Locate every Plasmodium parasite.
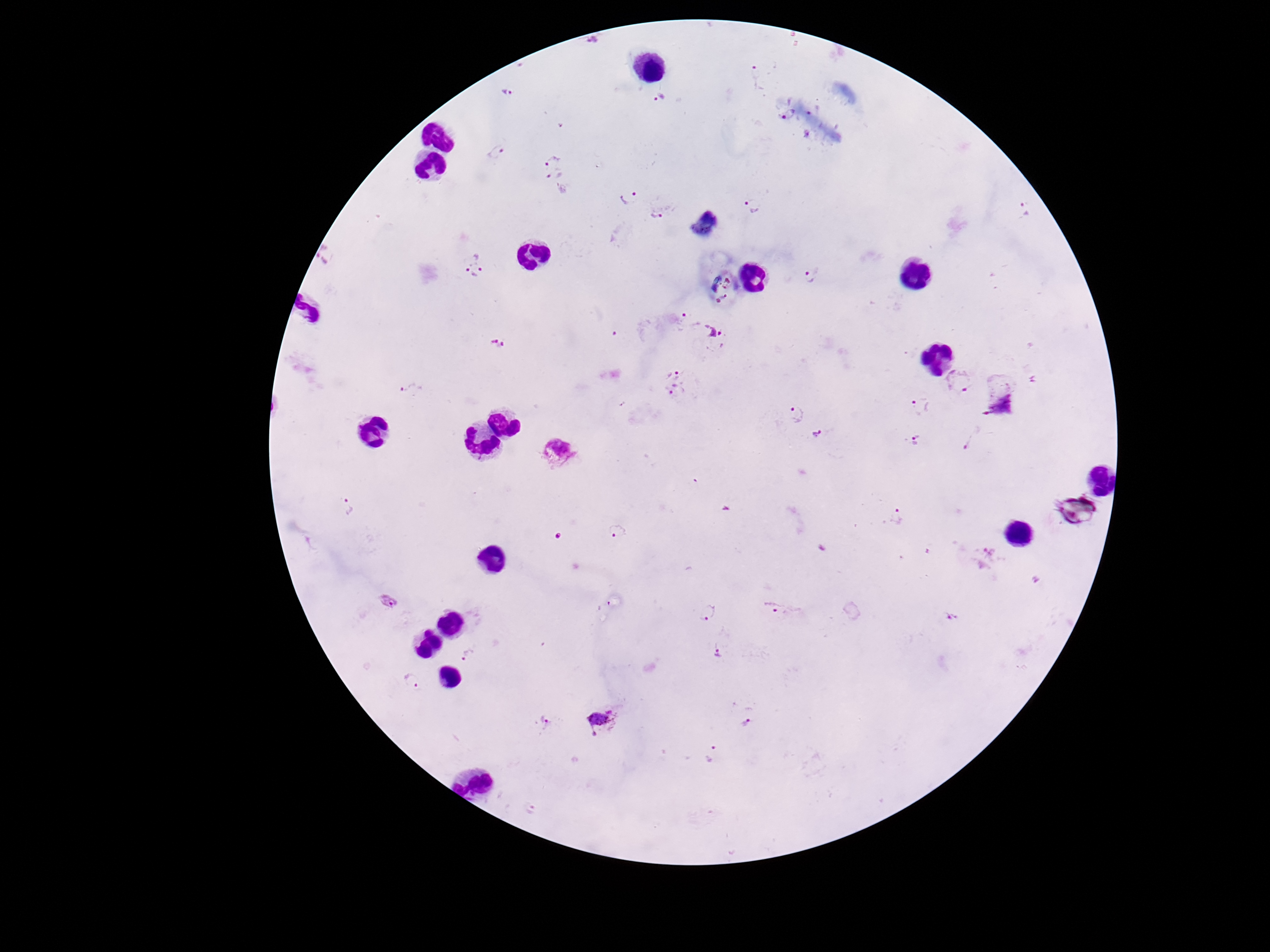

Approximate object centers, in pixels from the top-left corner.
Plasmodium parasites: (x=756, y=75), (x=506, y=92), (x=659, y=97), (x=789, y=113), (x=496, y=152), (x=552, y=160), (x=553, y=174), (x=561, y=190), (x=630, y=197), (x=754, y=204), (x=1026, y=208), (x=659, y=211), (x=331, y=255), (x=475, y=264), (x=810, y=276), (x=687, y=320), (x=718, y=337), (x=499, y=344), (x=674, y=370), (x=960, y=381), (x=413, y=390), (x=678, y=390), (x=921, y=407), (x=797, y=415), (x=819, y=432), (x=971, y=437), (x=918, y=442), (x=349, y=506), (x=897, y=517), (x=619, y=530), (x=1035, y=580), (x=390, y=601), (x=780, y=609), (x=707, y=612), (x=951, y=615), (x=719, y=652), (x=468, y=654), (x=413, y=681), (x=602, y=721), (x=545, y=722), (x=747, y=723), (x=711, y=752), (x=530, y=808).

Summary:
  - Capture: smartphone camera through the microscope eyepiece
  - Image size: 1270×952 pixels
  - Preparation: thick peripheral-blood smear
  - Patient malaria status: positive
  - Stain: Giemsa
  - Magnification: 100x
  - Field of view: one from this slide